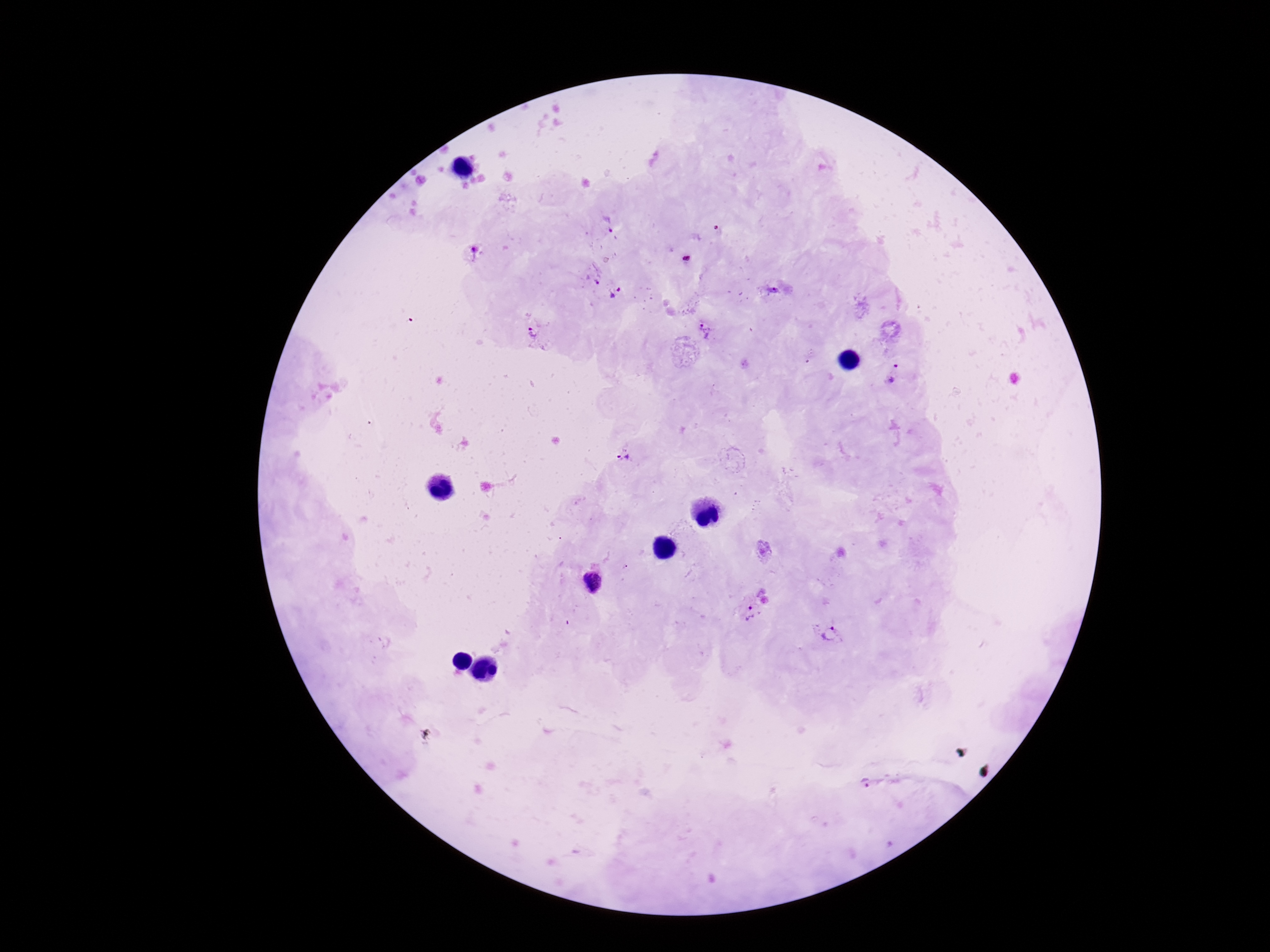
Approximate centers as {x, y} in pixels.
Summary:
  - Plasmodium parasite locations: {604, 226}, {475, 251}, {687, 258}, {590, 277}, {772, 289}, {615, 294}, {704, 330}, {535, 332}, {894, 373}, {625, 456}, {592, 583}, {753, 614}, {829, 634}, {867, 784}
  - Field of view: one from this slide
  - Magnification: 100x
  - Image size: 1270×952 pixels
  - Patient malaria status: positive
  - Preparation: thick peripheral-blood smear
  - Capture: smartphone camera through the microscope eyepiece
  - Stain: Giemsa